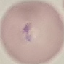

result = malaria parasites identified
image type = cell patch, automatically extracted from a larger field of view and resized to 64 × 64 pixels
capture = smartphone through the microscope eyepiece
stain = Giemsa
preparation = thin blood smear